Give the position of each Plasmodium falciparum parasite with its life-cycle stage, each leukocyte, and any debris.
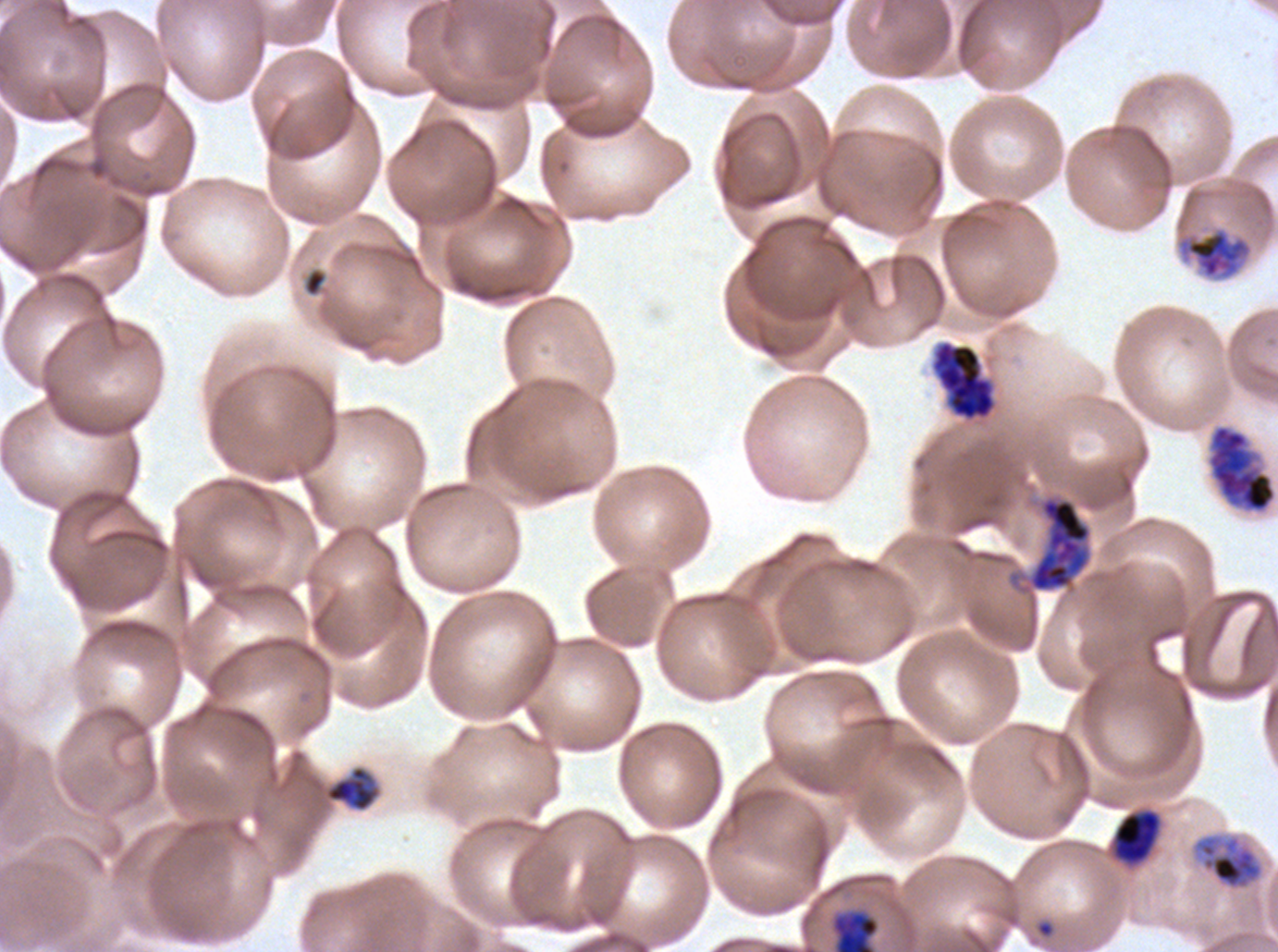

Approximate bounding boxes as (x1, y1, x2, y2) in pixels.
Late-ring/early-trophozoite forms: (325, 765, 380, 812).
Mid trophozoites: (1113, 811, 1160, 863).
Late trophozoites: (1178, 227, 1252, 279), (1192, 834, 1264, 891).
Early schizonts: (931, 341, 996, 421), (1206, 423, 1277, 514), (1029, 498, 1090, 592).
Debris: (302, 267, 327, 298).
One object is labeled both ring and mid trophozoite by the source: (829, 909, 880, 951).
No late schizonts, segmenters, gametocytes, or leukocytes observed.

stain = Giemsa
life-cycle stages observed = late-ring/early-trophozoite, mid trophozoite, late trophozoite, early schizont
image size = 1278×952 pixels
specimen = Plasmodium falciparum from a patient in The Gambia, cultured ex vivo for 24 to 48 hours
preparation = thin blood film
field of view = sub-image separated from a larger composite